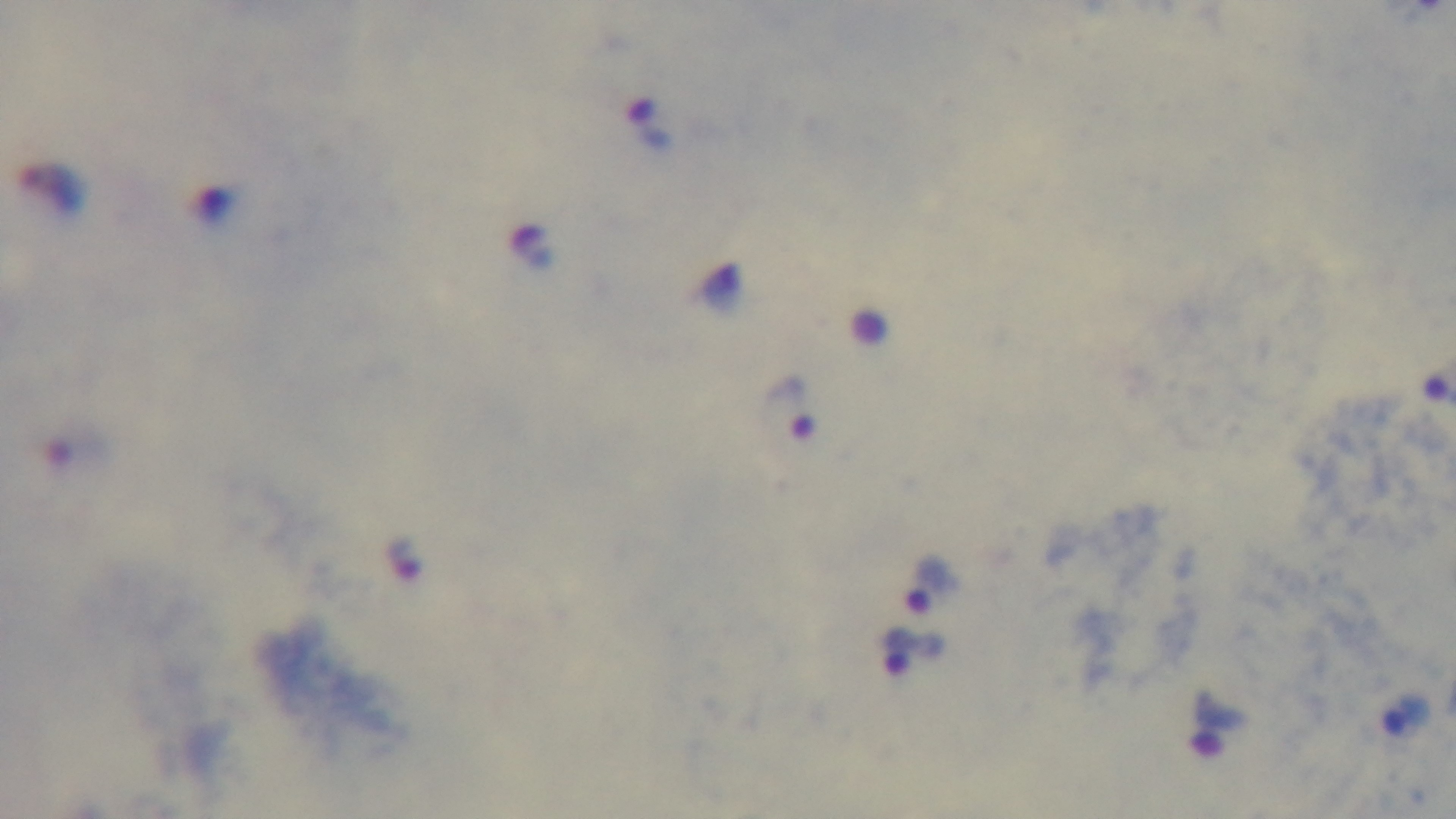

Summary:
  - Preparation: thick blood film
  - Field of view: one from the slide
  - Stain: Giemsa
  - Objective: 100x oil immersion
  - Capture: mounted 4K digital camera
  - Malaria status: positive
  - Modality: light microscopy